Give the extent of all uninfected red blood cells.
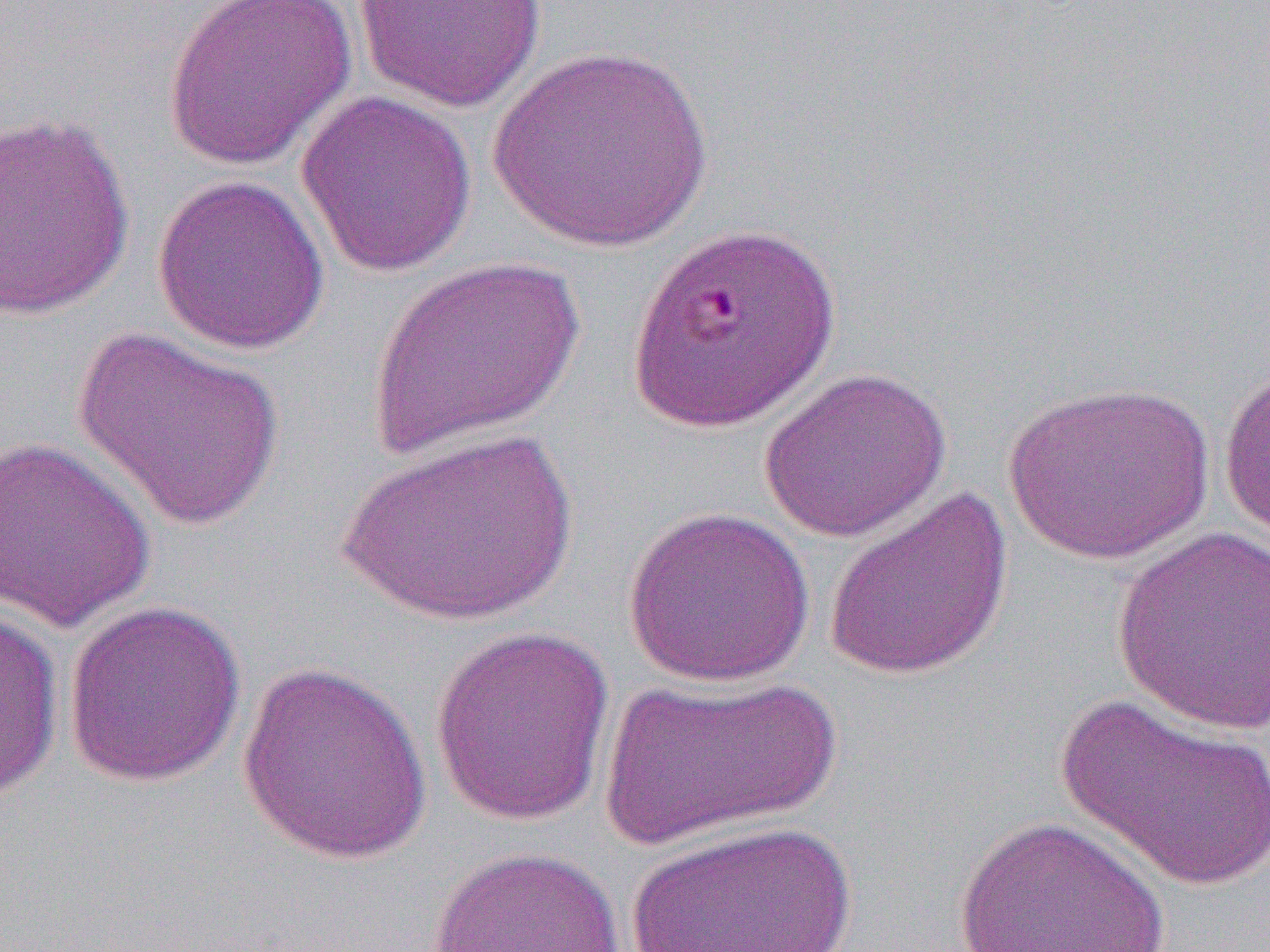

Approximate bounding boxes as [x1, y1, x2, y2] in pixels.
Uninfected red blood cells: [353, 0, 548, 113], [162, 1, 357, 172], [488, 45, 713, 254], [296, 90, 477, 278], [0, 111, 136, 320], [152, 174, 330, 355], [367, 256, 584, 464], [72, 324, 285, 531], [1219, 359, 1270, 547], [758, 367, 952, 543], [1003, 379, 1214, 564], [337, 428, 578, 627], [0, 434, 158, 632], [822, 486, 1015, 683], [623, 506, 817, 687], [1111, 526, 1270, 735], [62, 599, 246, 787], [0, 607, 65, 802], [429, 624, 617, 826], [236, 659, 434, 865], [597, 675, 842, 853], [1056, 692, 1270, 892], [953, 814, 1173, 952], [630, 818, 856, 952], [425, 845, 626, 951].

Slide-level diagnosis: Plasmodium falciparum. 1000x magnification. Single field of view. Image is 1270×952 pixels. Thin blood smear. Light microscopy.